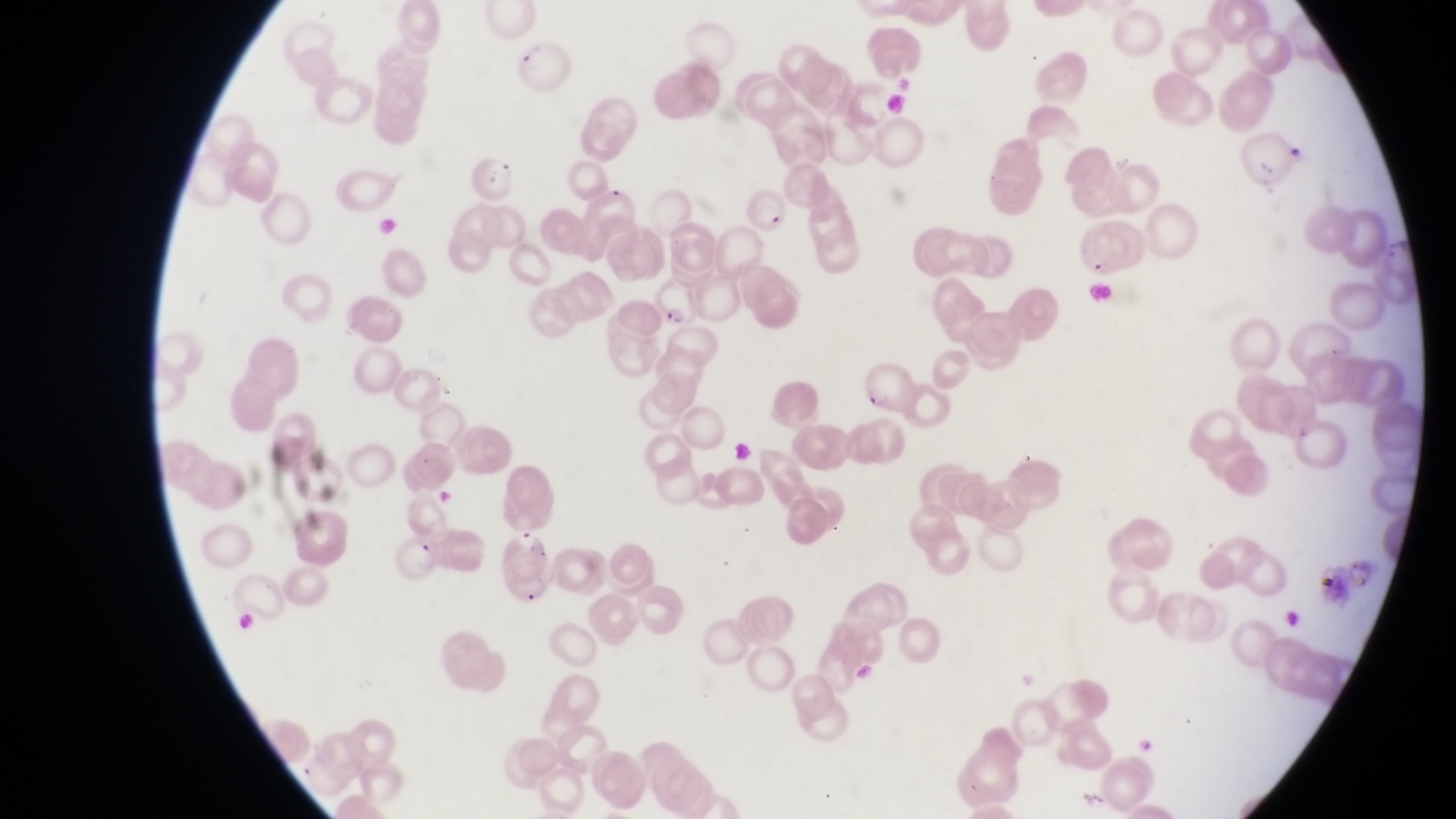
parasitised_red_blood_cell_locations: 'approximate bounding boxes as [left, top, right, bottom] in pixels: [515, 46, 578, 93], [737, 182, 787, 235], [1073, 221, 1149, 279], [657, 278, 699, 328], [859, 363, 914, 412], [495, 525, 561, 608]'
artifact_platelet_like_body_stain_precipitate_or_debris_locations: 'approximate bounding boxes as [left, top, right, bottom] in pixels: [492, 152, 521, 181]'
capture: smartphone photograph through the eyepiece of an Olympus CX-23 microscope
image_size: 1456×819 pixels
magnification: 1000x
field_of_view: single
preparation: thin blood film
country: Uganda